State the blood parasite species.
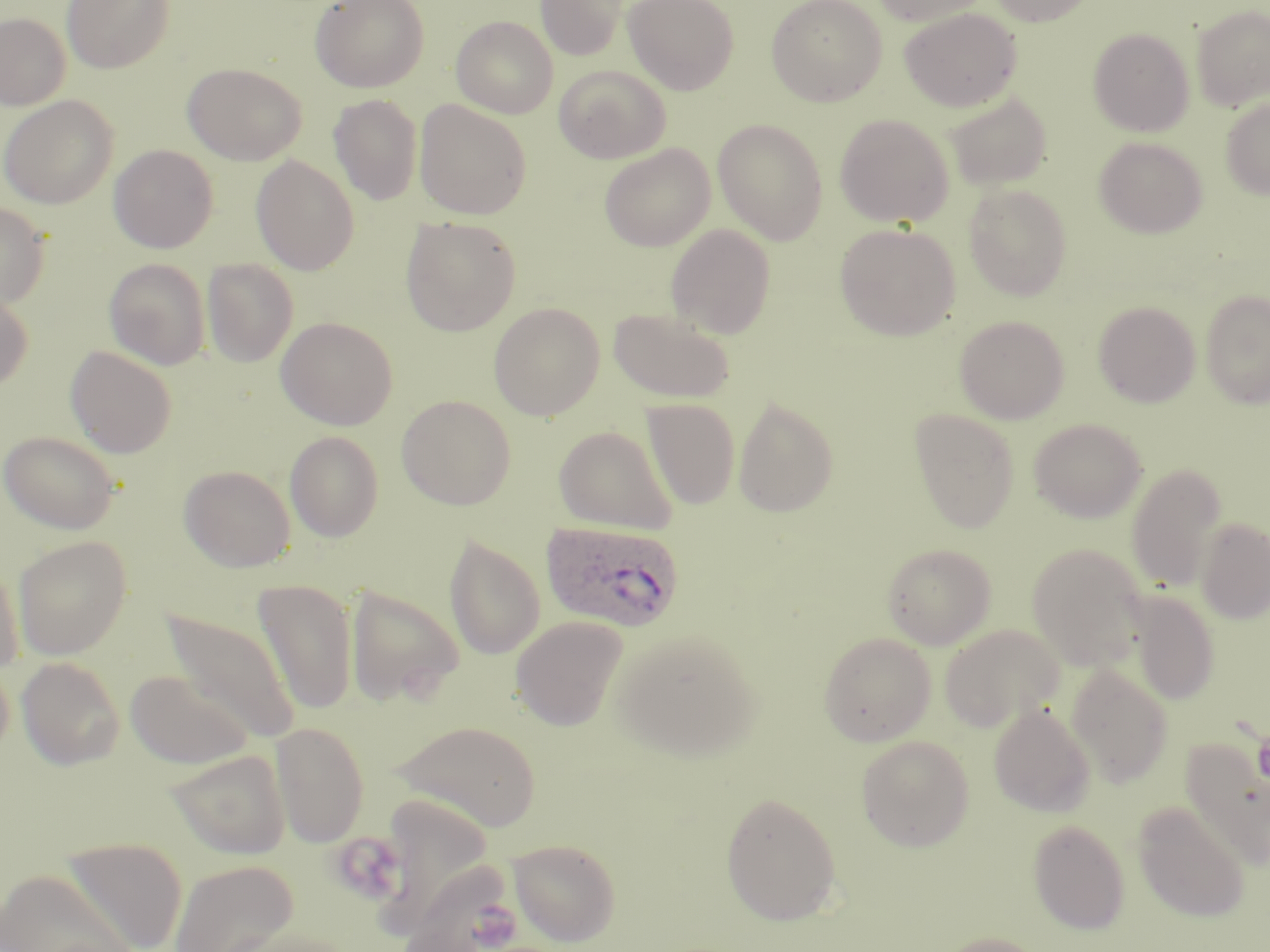

Plasmodium ovale.

Summary:
  - Coordinate format: approximate bounding boxes as named x1/y1/x2/y2 corners in pixels
  - Plasmodium ovale-infected red blood cell locations: (x1=540, y1=520, x2=684, y2=633)
  - Uninfected red blood cell locations: (x1=62, y1=0, x2=174, y2=74), (x1=310, y1=0, x2=429, y2=92), (x1=535, y1=0, x2=629, y2=60), (x1=624, y1=0, x2=738, y2=95), (x1=766, y1=0, x2=887, y2=106), (x1=869, y1=0, x2=993, y2=26), (x1=986, y1=0, x2=1099, y2=27), (x1=1191, y1=5, x2=1270, y2=111), (x1=900, y1=7, x2=1022, y2=111), (x1=0, y1=12, x2=71, y2=110), (x1=451, y1=15, x2=558, y2=118), (x1=1087, y1=28, x2=1194, y2=136), (x1=183, y1=62, x2=306, y2=165), (x1=554, y1=65, x2=670, y2=163), (x1=944, y1=92, x2=1053, y2=191), (x1=0, y1=95, x2=118, y2=209), (x1=329, y1=95, x2=423, y2=205), (x1=1220, y1=97, x2=1270, y2=200), (x1=414, y1=100, x2=532, y2=220), (x1=834, y1=113, x2=954, y2=227), (x1=713, y1=118, x2=829, y2=245), (x1=1094, y1=136, x2=1207, y2=238), (x1=599, y1=143, x2=716, y2=252), (x1=108, y1=144, x2=218, y2=253), (x1=251, y1=155, x2=360, y2=275), (x1=963, y1=184, x2=1073, y2=300), (x1=0, y1=202, x2=50, y2=307), (x1=400, y1=216, x2=521, y2=336), (x1=666, y1=223, x2=776, y2=338), (x1=834, y1=223, x2=960, y2=340), (x1=104, y1=258, x2=210, y2=369), (x1=202, y1=258, x2=298, y2=367), (x1=0, y1=286, x2=33, y2=393), (x1=1200, y1=289, x2=1270, y2=408), (x1=1093, y1=301, x2=1201, y2=407), (x1=489, y1=302, x2=605, y2=420), (x1=608, y1=307, x2=735, y2=402), (x1=954, y1=315, x2=1070, y2=423), (x1=276, y1=316, x2=398, y2=430), (x1=65, y1=346, x2=177, y2=458), (x1=396, y1=394, x2=516, y2=510), (x1=733, y1=397, x2=838, y2=518), (x1=641, y1=399, x2=740, y2=510), (x1=909, y1=409, x2=1020, y2=533), (x1=1029, y1=418, x2=1147, y2=523), (x1=554, y1=425, x2=677, y2=535), (x1=1, y1=430, x2=121, y2=534), (x1=285, y1=430, x2=384, y2=542), (x1=1126, y1=463, x2=1228, y2=592), (x1=178, y1=464, x2=296, y2=572), (x1=1196, y1=517, x2=1270, y2=624), (x1=444, y1=534, x2=545, y2=660), (x1=13, y1=535, x2=132, y2=660), (x1=881, y1=543, x2=997, y2=649), (x1=1026, y1=543, x2=1149, y2=670), (x1=0, y1=551, x2=26, y2=675), (x1=252, y1=578, x2=359, y2=716), (x1=345, y1=585, x2=464, y2=708), (x1=1128, y1=591, x2=1220, y2=705), (x1=161, y1=606, x2=300, y2=745), (x1=510, y1=616, x2=628, y2=731), (x1=939, y1=624, x2=1064, y2=731), (x1=613, y1=629, x2=762, y2=760), (x1=818, y1=631, x2=936, y2=746), (x1=16, y1=656, x2=125, y2=770), (x1=1066, y1=664, x2=1173, y2=786), (x1=125, y1=670, x2=254, y2=769), (x1=988, y1=704, x2=1095, y2=817), (x1=393, y1=719, x2=542, y2=831), (x1=270, y1=721, x2=370, y2=847), (x1=856, y1=735, x2=974, y2=851), (x1=1181, y1=737, x2=1270, y2=870), (x1=165, y1=747, x2=292, y2=859), (x1=720, y1=791, x2=842, y2=925), (x1=1133, y1=802, x2=1250, y2=922), (x1=1028, y1=820, x2=1130, y2=934), (x1=62, y1=836, x2=188, y2=951), (x1=509, y1=837, x2=621, y2=946), (x1=170, y1=858, x2=297, y2=952), (x1=400, y1=858, x2=515, y2=952), (x1=0, y1=866, x2=140, y2=952), (x1=225, y1=928, x2=359, y2=952), (x1=935, y1=931, x2=1047, y2=952)
  - Modality: light microscopy
  - Image size: 1270×952 pixels
  - Magnification: 1000x
  - Field of view: one of a larger specimen
  - Stain: May-Grünwald-Giemsa
  - Preparation: thin blood film